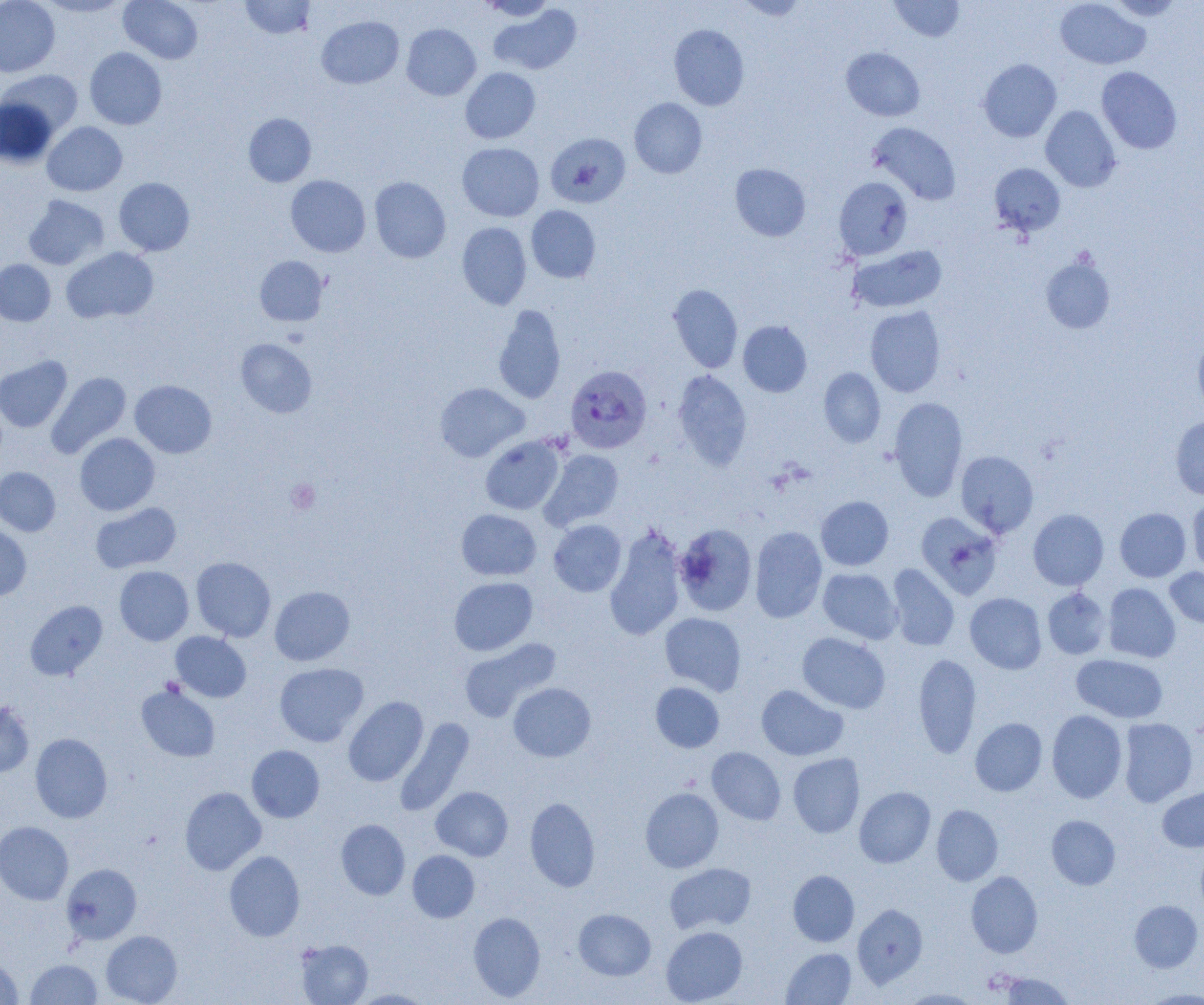
slide_level_diagnosis: Plasmodium falciparum
image_size: 1204×1005 pixels
plasmodium_falciparum_infected_red_blood_cell_locations: 'approximate bounding boxes as (x1, y1, x2, y2) in pixels: (565, 365, 652, 453)'
uninfected_red_blood_cell_locations: 'approximate bounding boxes as (x1, y1, x2, y2) in pixels: (0, 0, 60, 77), (37, 0, 130, 18), (119, 0, 203, 64), (478, 0, 556, 21), (736, 0, 810, 20), (889, 0, 965, 42), (1054, 0, 1150, 70), (1106, 0, 1186, 21), (240, 1, 315, 39), (488, 4, 582, 75), (316, 16, 404, 89), (402, 24, 481, 100), (668, 24, 749, 110), (85, 47, 167, 129), (840, 47, 925, 121), (978, 58, 1061, 142), (1096, 67, 1182, 154), (460, 68, 540, 144), (1, 70, 83, 137), (0, 98, 57, 168), (629, 98, 707, 178), (1040, 106, 1121, 191), (243, 113, 316, 187), (42, 122, 127, 196), (867, 122, 961, 205), (545, 133, 631, 208), (457, 143, 544, 221), (730, 163, 811, 241), (989, 163, 1065, 236), (285, 175, 371, 257), (369, 176, 451, 263), (834, 177, 913, 260), (114, 178, 195, 255), (23, 195, 109, 270), (526, 205, 601, 283), (457, 222, 531, 309), (848, 245, 947, 314), (61, 247, 158, 323), (1041, 255, 1115, 334), (254, 256, 328, 326), (0, 259, 55, 326), (668, 284, 743, 372), (493, 304, 566, 404), (865, 306, 946, 398), (738, 320, 812, 397), (1193, 334, 1204, 414), (236, 339, 317, 418), (0, 355, 72, 432), (818, 367, 886, 447), (672, 370, 752, 471), (47, 372, 131, 458), (130, 380, 217, 458), (435, 383, 529, 462), (889, 397, 968, 501), (1170, 415, 1204, 500), (74, 433, 160, 516), (480, 435, 565, 515), (539, 449, 624, 531), (956, 450, 1038, 537), (0, 467, 60, 536), (815, 496, 894, 571), (1187, 496, 1204, 576), (90, 502, 181, 573), (1115, 508, 1191, 582), (456, 509, 541, 580), (1028, 509, 1109, 590), (916, 512, 1004, 599), (548, 519, 627, 596), (674, 523, 757, 616), (0, 524, 32, 601), (749, 526, 827, 623), (604, 527, 687, 640), (191, 556, 276, 641), (887, 564, 959, 651), (114, 566, 194, 645), (1165, 567, 1204, 629), (817, 568, 902, 644), (449, 577, 537, 656), (1103, 583, 1180, 662), (269, 586, 355, 666), (1042, 588, 1111, 659), (965, 592, 1047, 674), (25, 600, 107, 680), (660, 612, 746, 695), (171, 631, 251, 702), (797, 632, 890, 714), (458, 638, 560, 722), (913, 652, 981, 759), (1071, 654, 1167, 723), (274, 663, 368, 747), (136, 682, 220, 762), (508, 682, 596, 762), (650, 682, 724, 752), (756, 685, 848, 760), (343, 696, 428, 787), (0, 701, 35, 778), (1047, 710, 1127, 803), (970, 717, 1047, 796), (395, 718, 475, 816), (1117, 718, 1198, 807), (30, 733, 112, 823), (247, 745, 324, 822), (707, 747, 786, 825), (788, 753, 865, 838), (431, 786, 513, 860), (854, 786, 935, 868), (1157, 786, 1204, 851), (180, 787, 265, 875), (640, 787, 724, 873), (525, 797, 601, 892), (931, 804, 1003, 886), (1046, 815, 1120, 889), (336, 819, 410, 899), (0, 821, 74, 905), (1196, 844, 1204, 919), (224, 850, 305, 941), (407, 850, 479, 922), (664, 862, 756, 934), (61, 863, 142, 945), (788, 870, 859, 946), (966, 871, 1043, 958), (1129, 900, 1203, 972), (852, 904, 928, 988), (574, 908, 656, 980), (468, 912, 545, 1001), (661, 926, 747, 1004), (101, 930, 182, 1004), (295, 939, 373, 1005), (781, 948, 856, 1004), (0, 957, 23, 1004), (26, 958, 102, 1004), (999, 972, 1076, 1004), (349, 988, 435, 1004), (900, 988, 984, 1004), (1141, 988, 1204, 1004)'
field_of_view: single
preparation: thin blood smear
magnification: 1000x
modality: light microscopy
platelet_locations: 'approximate bounding boxes as (x1, y1, x2, y2) in pixels: (285, 479, 320, 514)'